Identify the preparation type.
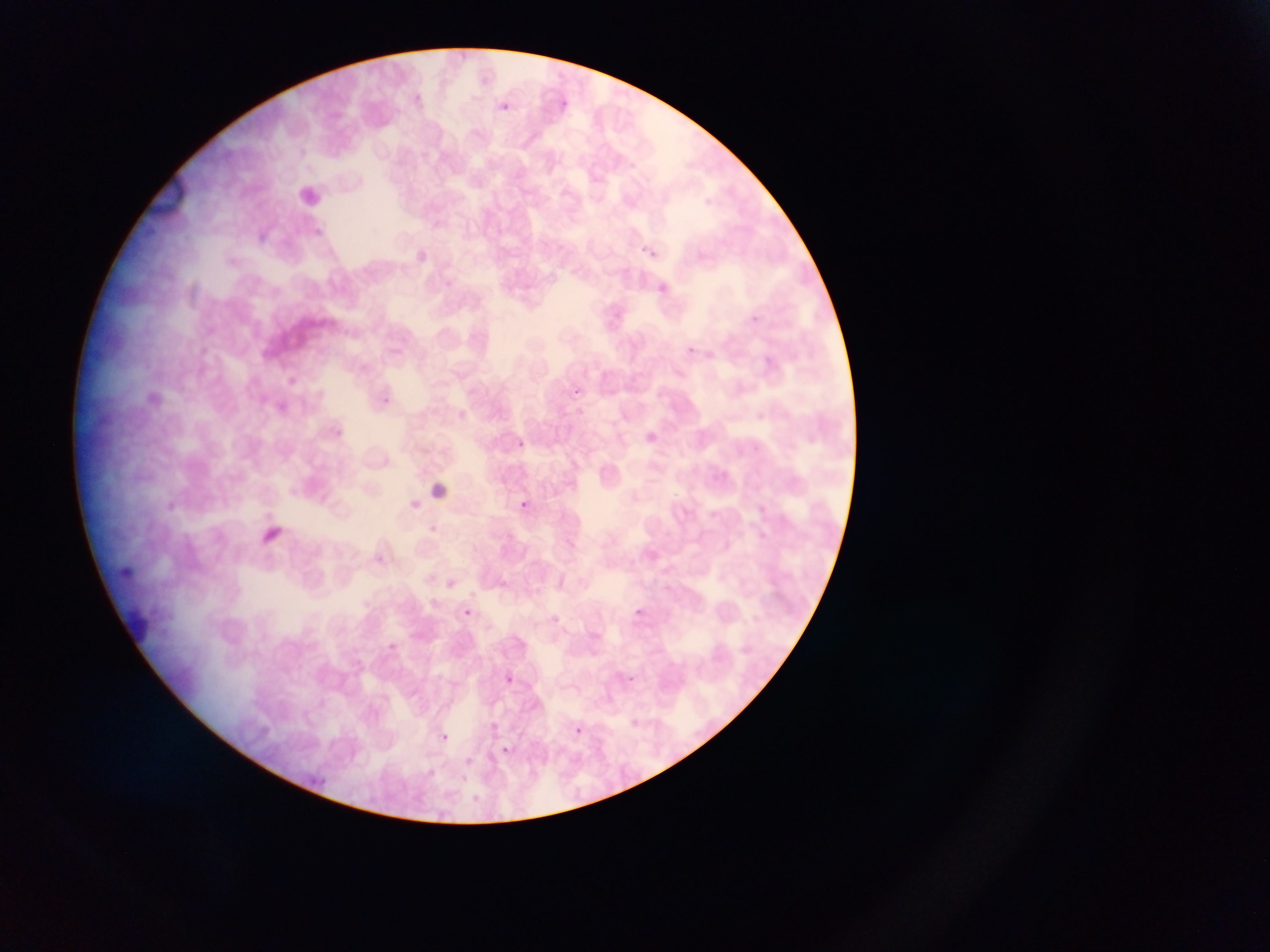

Thin blood smear.

Approximate bounding boxes as (left, top, right, bottom) in pixels. Plasmodium parasite locations: (558, 97, 573, 106), (502, 99, 514, 116), (641, 240, 662, 262), (657, 277, 664, 290), (199, 347, 207, 355), (288, 377, 297, 385), (516, 440, 524, 448), (288, 487, 297, 495), (521, 500, 529, 507), (264, 512, 272, 520), (276, 526, 285, 534), (429, 598, 438, 606), (629, 603, 650, 618), (463, 609, 471, 615), (389, 642, 397, 650), (626, 673, 641, 682), (506, 676, 514, 683), (260, 726, 269, 735), (569, 726, 587, 738), (435, 733, 455, 748), (504, 745, 514, 759). One field of view. Photographed through a microscope with a mobile-phone camera. Collected in Ghana. Image is 1270×952 pixels.